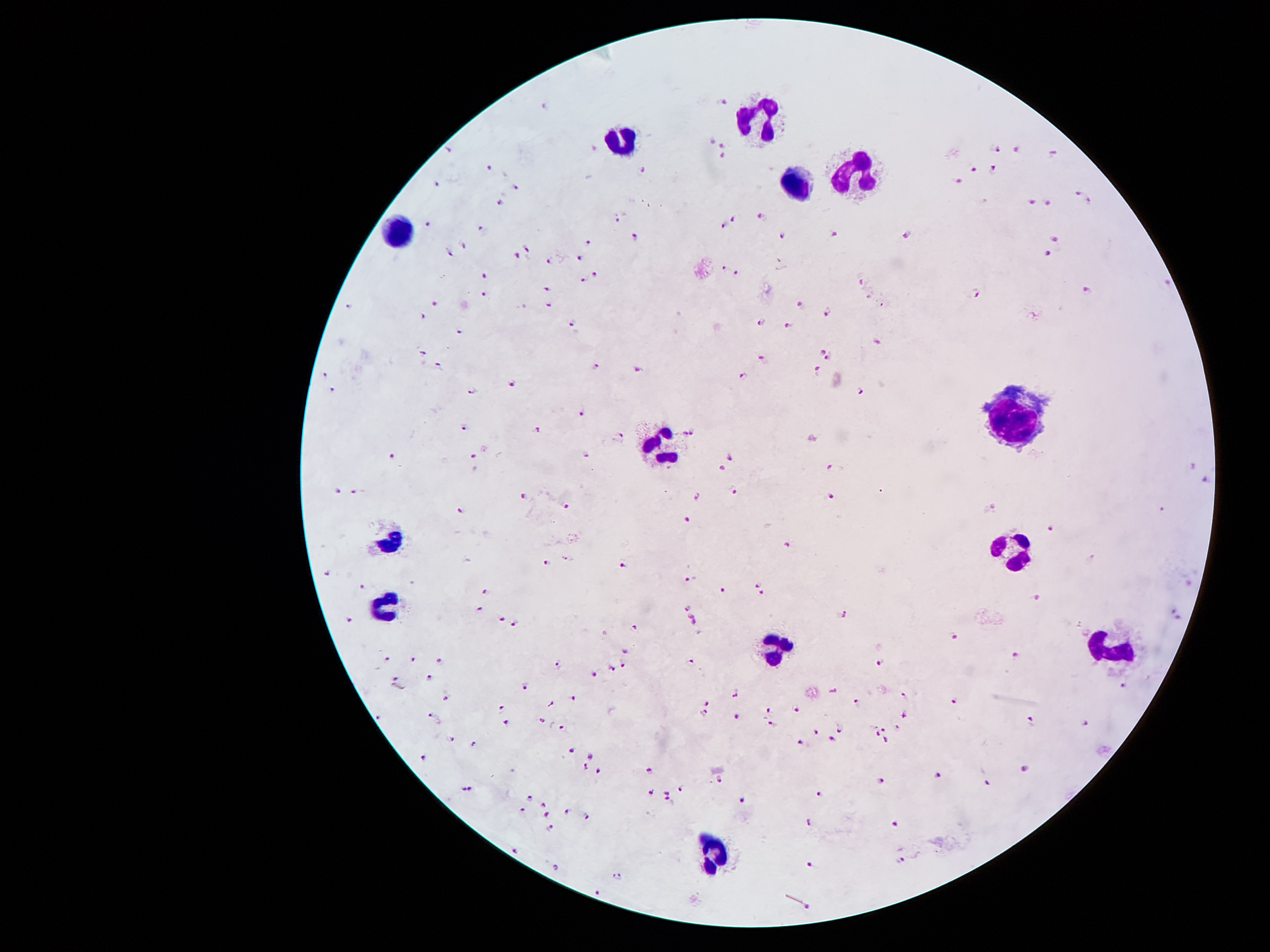

Image is 1270×952 pixels. 100x magnification. Single field of view. Thick blood smear. Photographed through the microscope eyepiece with a smartphone camera. Giemsa stain. Patient malaria status: positive for Plasmodium falciparum.